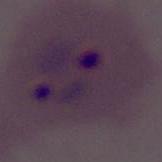

A Plasmodium parasite is seen. 400x or 1000x magnification. Photomicrograph.